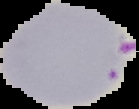
From a thin blood film. Cell region segmented out of the field of view; the surrounding area is masked to black. Image is 139×109 pixels. Result: Plasmodium parasites identified.